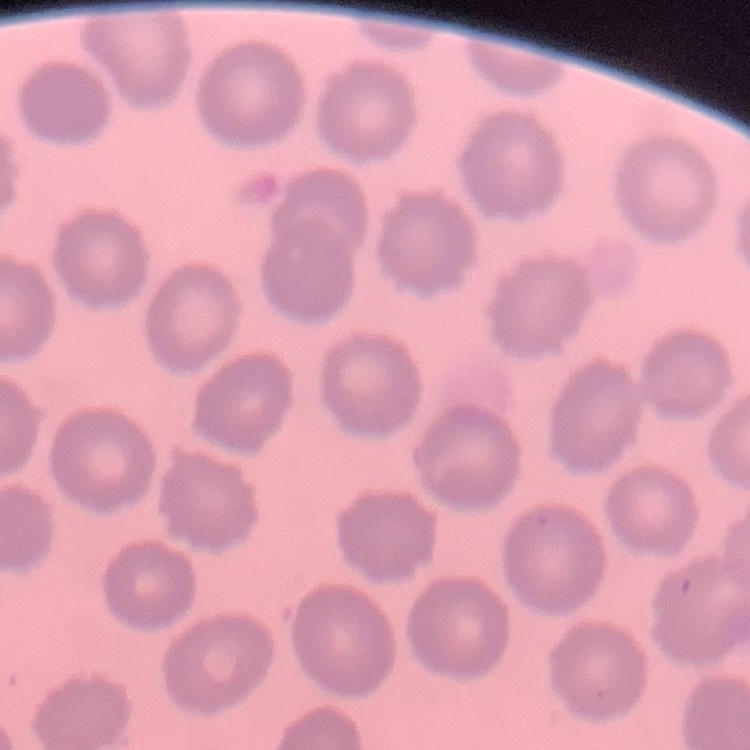
red_blood_cell_morphology: no rouleaux formation
stain: Field's or Giemsa
preparation: thin peripheral smear
image_type: one tile cut from a larger photomicrograph